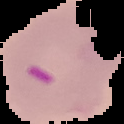

Summary:
  - Image size: 124×124 pixels
  - Image type: segmented cell region on a black background
  - Result: Plasmodium parasites detected
  - Preparation: thin blood smear